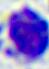
Summary:
  - Modality: micrograph
  - Magnification: 400x
  - Identification: leukocyte